Report the malaria status of this cell.
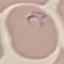
It is parasitized.

Summary:
  - Capture: smartphone through the microscope eyepiece
  - Preparation: thin blood film
  - Stain: Giemsa
  - Image type: cell patch, automatically extracted from a larger field of view and resized to 64 × 64 pixels